Give the position of every malaria parasite.
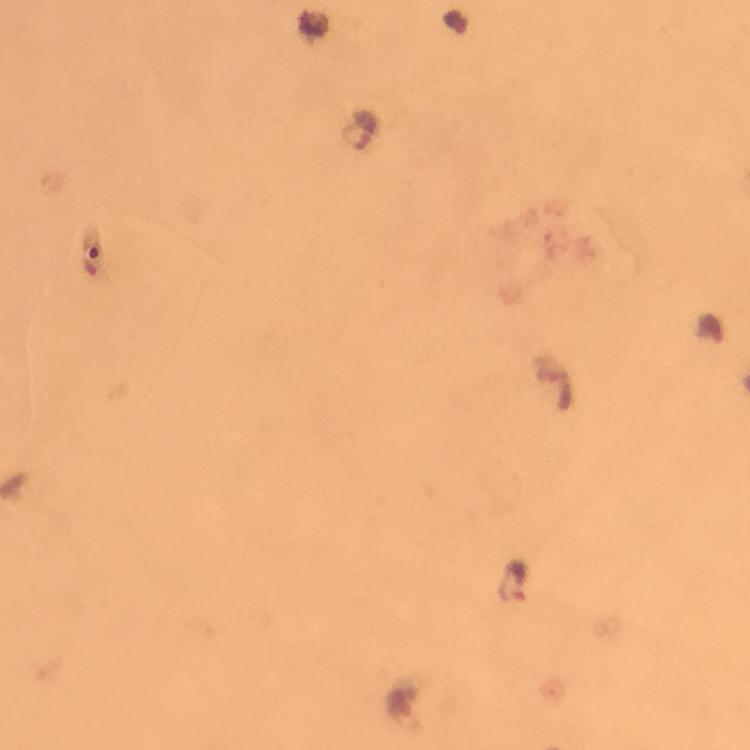

Approximate centers as {x, y} in pixels.
Malaria parasites: {363, 128}, {514, 582}.

Smartphone photograph taken through a microscope. Thick smear. From a diagnostic examination for malaria. Giemsa stain. Cropped region of a single field of view. 100x magnification. Immersion oil applied. Image is 750×750 pixels.